Locate every blood parasite and identify its species.
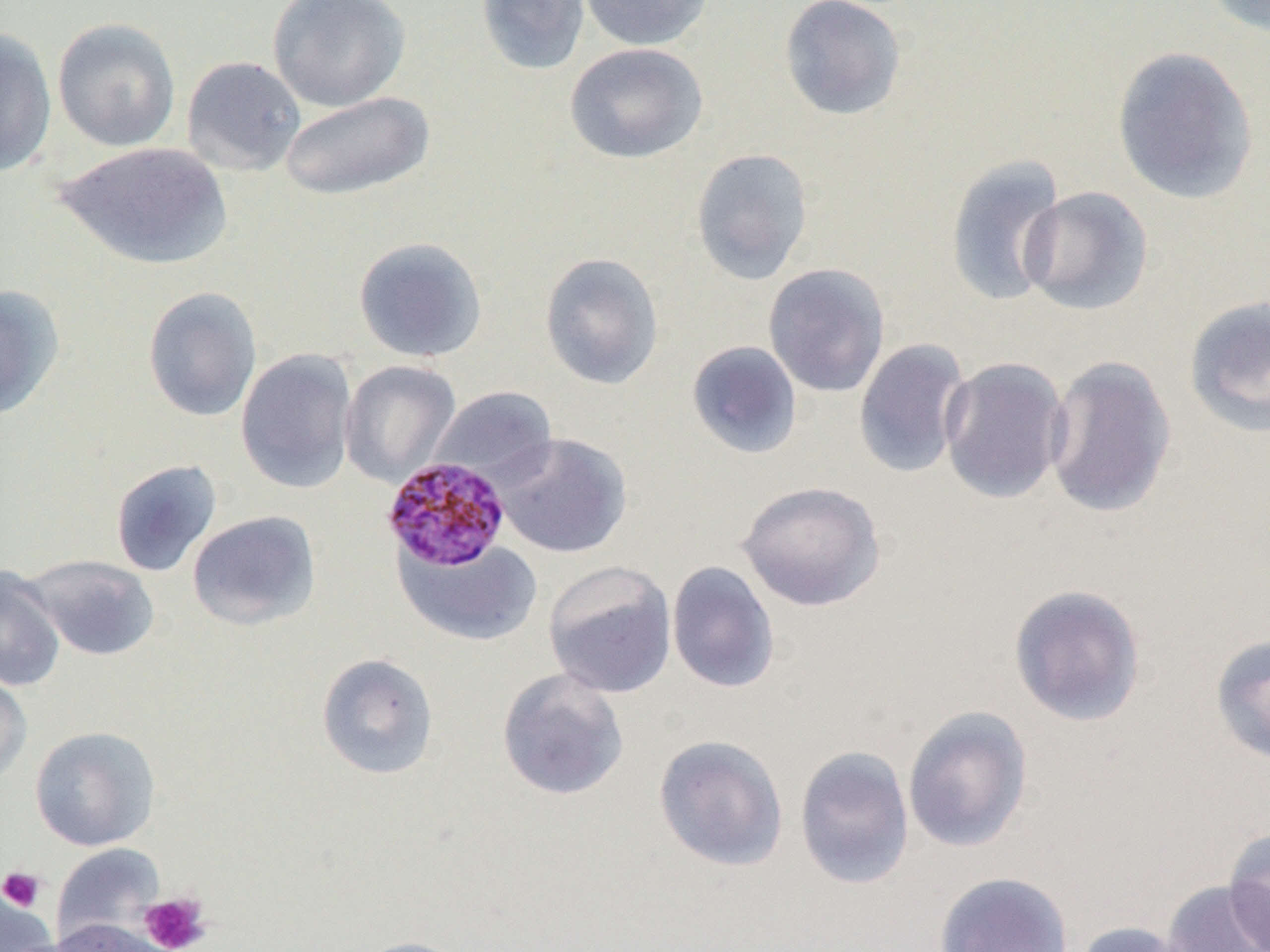
Approximate bounding boxes as named x1/y1/x2/y2 corners in pixels.
Plasmodium malariae-infected red blood cells: (x1=382, y1=456, x2=512, y2=572).
No Plasmodium falciparum, Plasmodium ovale, Plasmodium vivax, Babesia divergens, or Trypanosoma brucei observed.

Uninfected red blood cell locations (subset): (x1=267, y1=0, x2=411, y2=111), (x1=476, y1=0, x2=590, y2=75), (x1=578, y1=0, x2=715, y2=51), (x1=778, y1=0, x2=907, y2=121), (x1=1200, y1=0, x2=1270, y2=38), (x1=52, y1=17, x2=181, y2=152), (x1=0, y1=27, x2=57, y2=177), (x1=565, y1=42, x2=709, y2=164), (x1=1111, y1=45, x2=1259, y2=204), (x1=181, y1=55, x2=306, y2=176), (x1=279, y1=90, x2=435, y2=202), (x1=55, y1=141, x2=232, y2=271), (x1=690, y1=148, x2=813, y2=285), (x1=944, y1=155, x2=1067, y2=307), (x1=1018, y1=185, x2=1154, y2=316), (x1=353, y1=236, x2=487, y2=362), (x1=539, y1=252, x2=664, y2=390), (x1=763, y1=263, x2=890, y2=398), (x1=0, y1=283, x2=66, y2=421), (x1=143, y1=286, x2=262, y2=422), (x1=1183, y1=296, x2=1270, y2=438), (x1=853, y1=338, x2=973, y2=478), (x1=686, y1=340, x2=803, y2=459), (x1=236, y1=349, x2=358, y2=494), (x1=1043, y1=354, x2=1177, y2=519), (x1=939, y1=356, x2=1070, y2=505), (x1=339, y1=359, x2=461, y2=488), (x1=429, y1=387, x2=558, y2=488), (x1=494, y1=433, x2=631, y2=558), (x1=110, y1=459, x2=222, y2=578), (x1=736, y1=480, x2=887, y2=612), (x1=187, y1=510, x2=320, y2=630), (x1=397, y1=538, x2=543, y2=646), (x1=21, y1=554, x2=159, y2=661), (x1=543, y1=561, x2=677, y2=698), (x1=666, y1=561, x2=780, y2=694), (x1=0, y1=565, x2=66, y2=693), (x1=1008, y1=583, x2=1147, y2=727), (x1=1210, y1=633, x2=1270, y2=766), (x1=316, y1=653, x2=439, y2=779), (x1=497, y1=668, x2=629, y2=800), (x1=0, y1=670, x2=32, y2=786), (x1=901, y1=706, x2=1034, y2=854), (x1=30, y1=726, x2=161, y2=851), (x1=653, y1=734, x2=789, y2=872), (x1=794, y1=745, x2=915, y2=889), (x1=1223, y1=831, x2=1270, y2=950), (x1=51, y1=843, x2=165, y2=945), (x1=934, y1=871, x2=1074, y2=952), (x1=1159, y1=879, x2=1270, y2=952), (x1=0, y1=887, x2=53, y2=951), (x1=51, y1=918, x2=174, y2=952), (x1=1072, y1=920, x2=1197, y2=952), (x1=349, y1=936, x2=472, y2=952). Platelet locations (subset): (x1=139, y1=892, x2=212, y2=952). Slide-level diagnosis: Plasmodium malariae. One field of a larger specimen. Thin blood film. Optical microscopy. Image is 1270×952 pixels. Captured at 1000x magnification.